Assess the morphology of the erythrocytes.
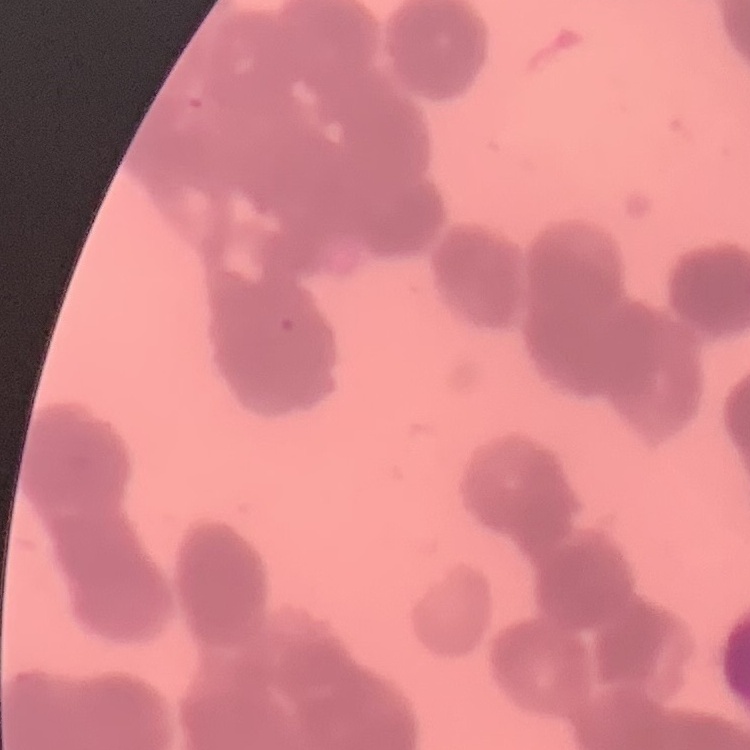

They show rouleaux formation.

stain = Field's or Giemsa
preparation = thin blood smear
image type = one tile cut from a larger photomicrograph